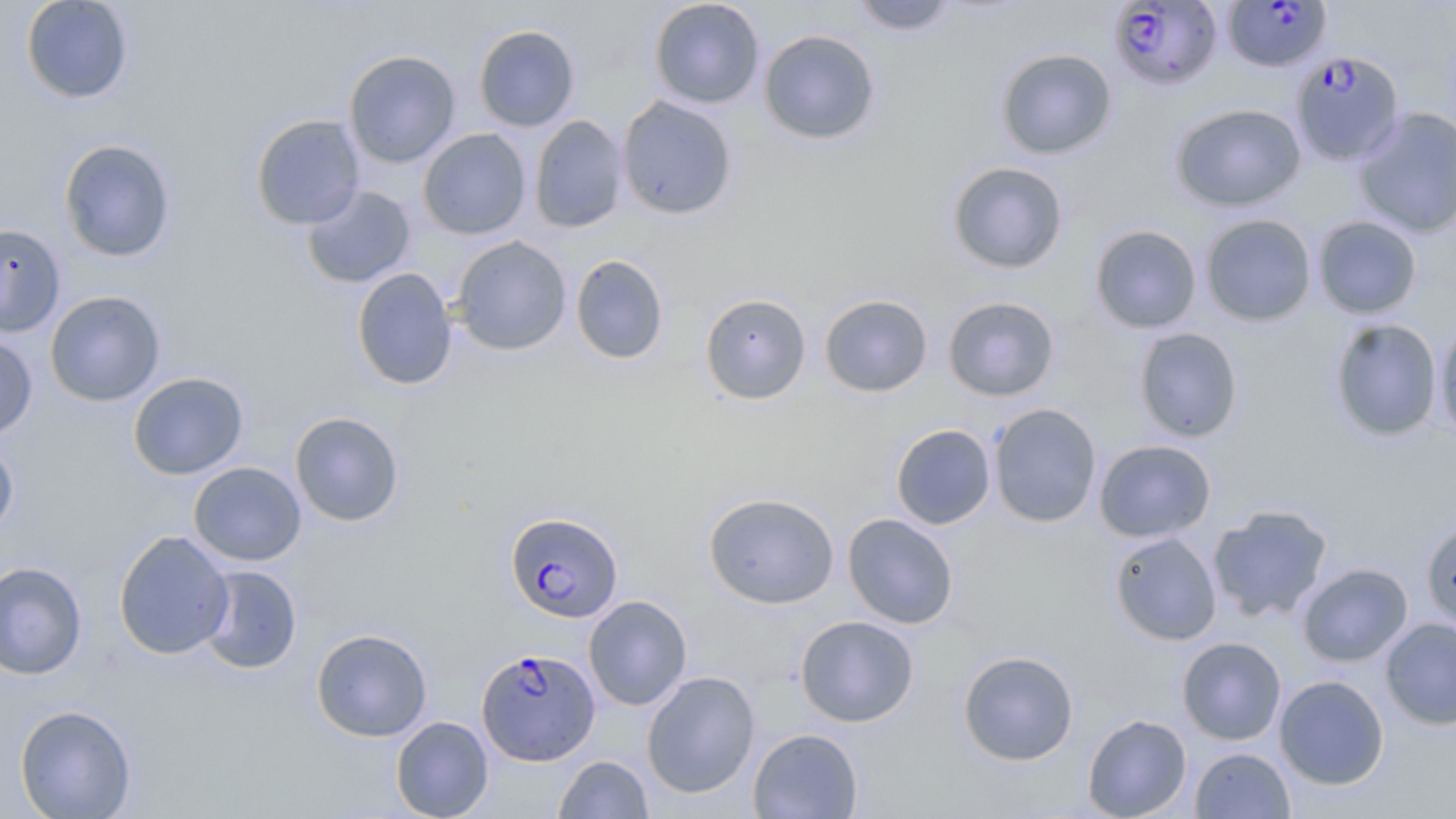
Approximate bounding boxes as [x1, y1, x2, y2] in pixels. Uninfected red blood cell locations: [20, 0, 134, 104], [649, 0, 765, 109], [850, 0, 957, 36], [473, 24, 580, 132], [758, 29, 881, 145], [996, 48, 1117, 159], [343, 49, 461, 168], [617, 95, 738, 220], [1170, 103, 1307, 211], [1353, 106, 1456, 238], [250, 114, 365, 229], [529, 115, 629, 233], [418, 128, 531, 240], [59, 139, 176, 262], [946, 161, 1069, 274], [301, 184, 416, 289], [1199, 213, 1317, 326], [1313, 215, 1422, 319], [0, 223, 66, 338], [1089, 224, 1202, 334], [452, 235, 572, 355], [570, 255, 669, 364], [352, 267, 457, 390], [45, 290, 166, 406], [700, 293, 811, 405], [819, 294, 933, 397], [942, 296, 1060, 402], [1434, 316, 1456, 444], [1329, 318, 1444, 442], [1133, 327, 1244, 443], [0, 334, 38, 440], [127, 372, 249, 480], [988, 403, 1103, 527], [289, 411, 404, 527], [890, 423, 996, 530], [0, 438, 19, 540], [1093, 439, 1216, 543], [188, 461, 307, 566], [703, 492, 840, 609], [1208, 504, 1333, 622], [842, 513, 959, 629], [1420, 518, 1456, 631], [113, 529, 234, 659], [1109, 531, 1222, 646], [0, 560, 88, 680], [1297, 562, 1413, 667], [195, 565, 302, 674], [583, 595, 692, 711], [795, 615, 919, 727], [1380, 618, 1456, 729], [311, 628, 433, 741], [1177, 636, 1287, 745], [958, 650, 1079, 765], [642, 671, 760, 798], [1274, 675, 1389, 790], [14, 703, 137, 818], [1082, 713, 1192, 818], [390, 716, 494, 819], [748, 728, 864, 818], [1190, 746, 1295, 818], [554, 755, 653, 818]. Plasmodium falciparum-infected red blood cell locations: [1221, 0, 1332, 74], [1110, 1, 1223, 90], [1291, 51, 1404, 166], [505, 511, 625, 623], [476, 647, 599, 765]. Slide-level diagnosis: Plasmodium falciparum. Thin blood film. Image is 1456×819 pixels. May-Grünwald-Giemsa stain. Optical microscopy. 1000x magnification. One field of a larger specimen.